Report the malaria status of this cell.
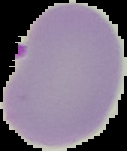

Parasitized.

Summary:
  - Preparation: thin blood smear
  - Image type: cell region segmented out of the field of view; surrounding area masked to black
  - Image size: 127×151 pixels